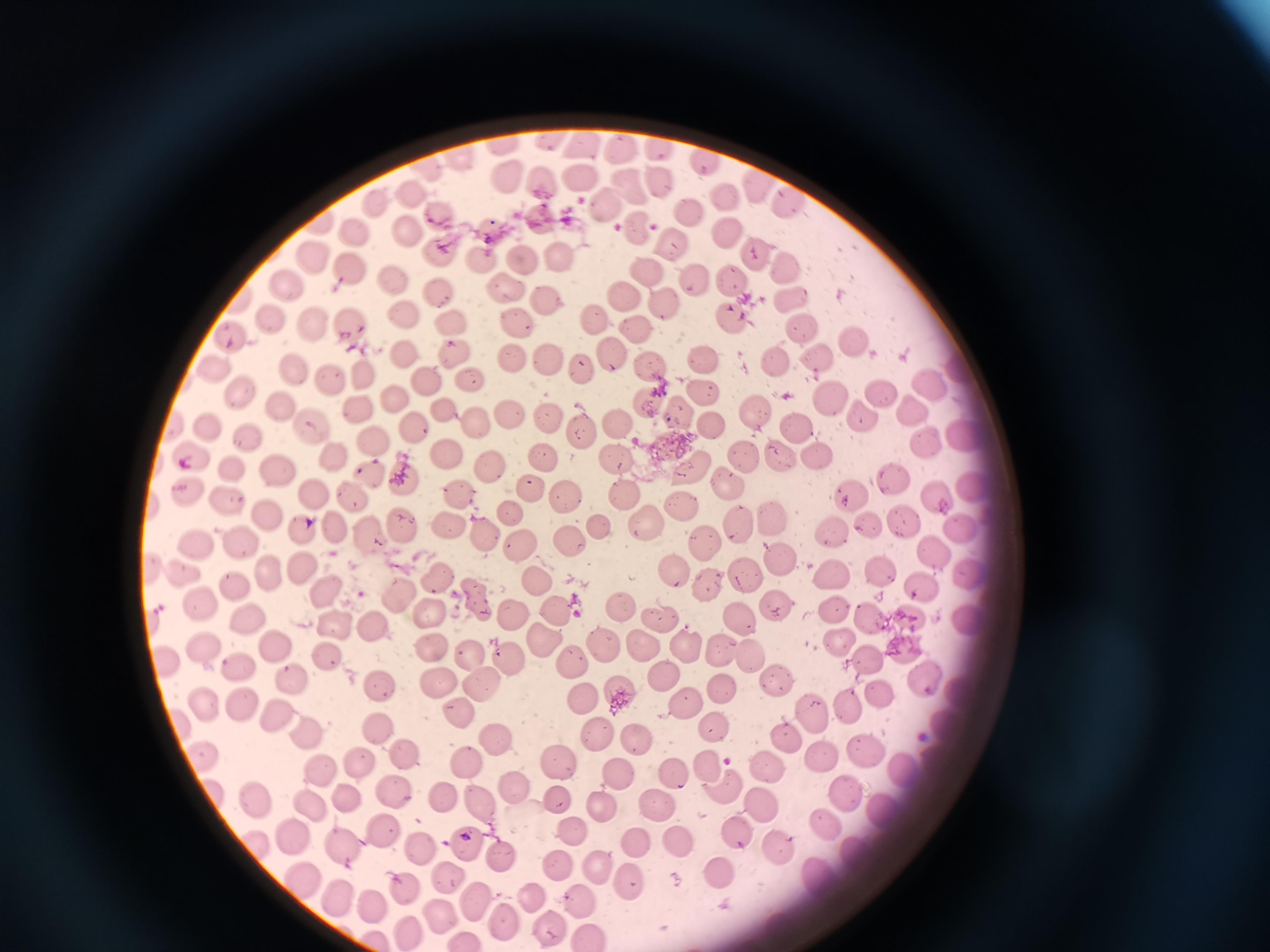

Approximate centers as [x, y] in pixels. Cell locations: [547, 140], [504, 141], [582, 146], [657, 149], [620, 151], [707, 159], [460, 160], [505, 177], [580, 177], [655, 177], [544, 180], [757, 182], [634, 187], [410, 192], [728, 192], [793, 202], [375, 203], [606, 206], [691, 211], [441, 212], [541, 216], [638, 225], [404, 227], [490, 228], [354, 232], [727, 233], [674, 242], [438, 247], [559, 252], [753, 253], [523, 255], [314, 259], [480, 260], [786, 263], [354, 270], [651, 270], [395, 276], [731, 276], [695, 279], [287, 284], [509, 285], [436, 286], [626, 294], [545, 298], [790, 298], [666, 304], [274, 314], [597, 314], [404, 316], [731, 316], [446, 318], [518, 324], [351, 325], [311, 326], [804, 327], [637, 330], [230, 331], [856, 337], [405, 347], [452, 351], [611, 351], [703, 355], [513, 356], [551, 356], [820, 358], [289, 361], [776, 363], [213, 366], [649, 366], [582, 367], [361, 375], [329, 377], [426, 379], [464, 381], [930, 381], [235, 389], [700, 391], [877, 393], [393, 395], [827, 398], [283, 401], [643, 401], [758, 408], [912, 409], [356, 411], [508, 412], [674, 414], [858, 414], [449, 415], [547, 417], [617, 421], [311, 423], [710, 423], [474, 424], [211, 425], [408, 426], [795, 427], [584, 428], [251, 434], [963, 434], [373, 439], [921, 441], [815, 453], [335, 454], [616, 454], [780, 454], [194, 455], [446, 455], [744, 455], [545, 459], [230, 462], [278, 466], [686, 466], [490, 469], [369, 474], [404, 476], [890, 477], [726, 478], [975, 483], [183, 487], [530, 489], [627, 490], [314, 491], [853, 491], [456, 492], [938, 493], [356, 495], [569, 497], [224, 500], [684, 505], [268, 511], [517, 511], [771, 518], [641, 519], [903, 519], [403, 522], [333, 523], [737, 524], [870, 524], [453, 525], [305, 527], [830, 527], [954, 527], [604, 528], [369, 535], [241, 536], [486, 537], [523, 541], [573, 541], [195, 545], [702, 545], [931, 550], [779, 557], [301, 564], [883, 568], [745, 569], [676, 570], [268, 571], [968, 571], [828, 572], [439, 573], [534, 573], [183, 574], [234, 583], [708, 584], [327, 588], [917, 588], [399, 593], [476, 597], [621, 601], [775, 602], [203, 605], [831, 605], [556, 606], [429, 609], [510, 611], [875, 616], [659, 617], [742, 617], [251, 618], [909, 618], [970, 619], [335, 626], [373, 631], [543, 639], [201, 644], [429, 644], [639, 644], [689, 644], [838, 644], [276, 645], [722, 646], [603, 647], [904, 647], [470, 654], [752, 656], [866, 656], [327, 657], [161, 659], [507, 659], [574, 660], [238, 667], [661, 673], [292, 675], [923, 679], [436, 682], [380, 683], [778, 683], [482, 686], [721, 687], [879, 689], [621, 692], [582, 694], [685, 701], [852, 702], [241, 703], [208, 704], [460, 713], [273, 714], [811, 714], [381, 728], [712, 728], [306, 730], [596, 735], [494, 738], [784, 738], [634, 739], [865, 742], [821, 755], [198, 756], [408, 757], [556, 760], [359, 762], [465, 762], [318, 767], [707, 767], [769, 767], [902, 767], [616, 770], [675, 772], [724, 786], [395, 787], [513, 789], [846, 792], [343, 795], [446, 796], [477, 796], [558, 799], [249, 800], [600, 801], [659, 801], [313, 806], [886, 806], [762, 807], [822, 822], [379, 827], [735, 828], [569, 830], [292, 839], [679, 840], [464, 841], [635, 841], [419, 842], [249, 843], [341, 844], [780, 850], [858, 851], [500, 858], [556, 863], [596, 864], [817, 873], [719, 874], [444, 877], [628, 878], [306, 880], [403, 884], [531, 894], [471, 897], [338, 898], [586, 901], [370, 906], [439, 917], [506, 919], [550, 927], [410, 929], [591, 933], [465, 940]. Image is 1270×952 pixels. Acquired by smartphone through the microscope eyepiece. Giemsa stain. Thin blood smear. Single field of view.